Assess this cell for malaria.
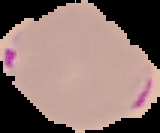

Parasitized.

Segmented cell region on a black background. From a thin blood film. Image is 160×133 pixels.